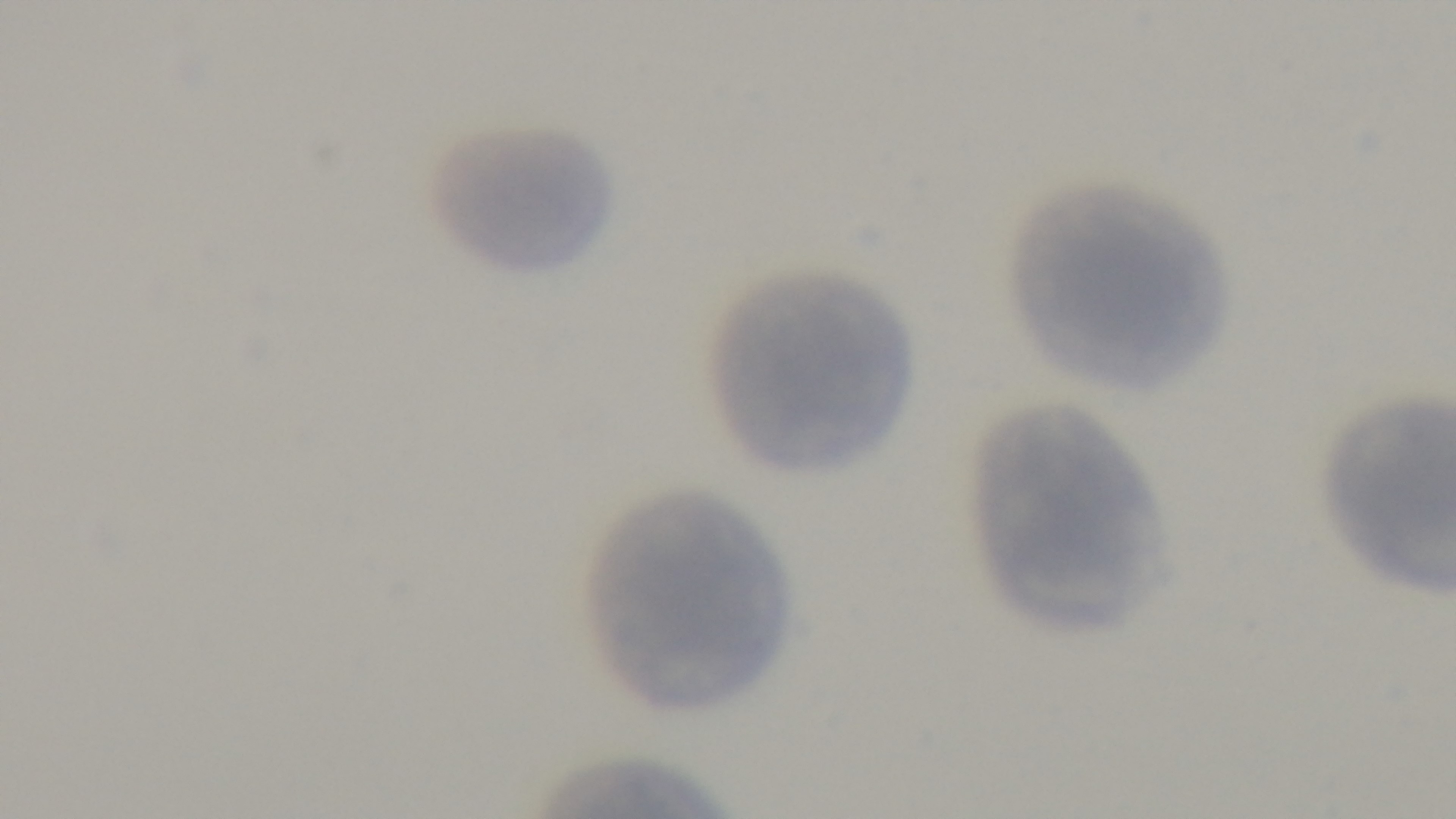
Preparation: thin smear. Malaria status: negative. Single field of view. 100x oil-immersion objective. Giemsa stain. Captured with a mounted 4K digital camera. Light microscopy.